Classify this cell by malaria status.
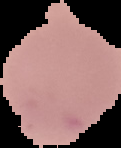
Uninfected.

image type = cell region segmented out of the field of view; surrounding area masked to black
preparation = thin blood film
image size = 121×148 pixels